Assess the morphology of the red blood cells.
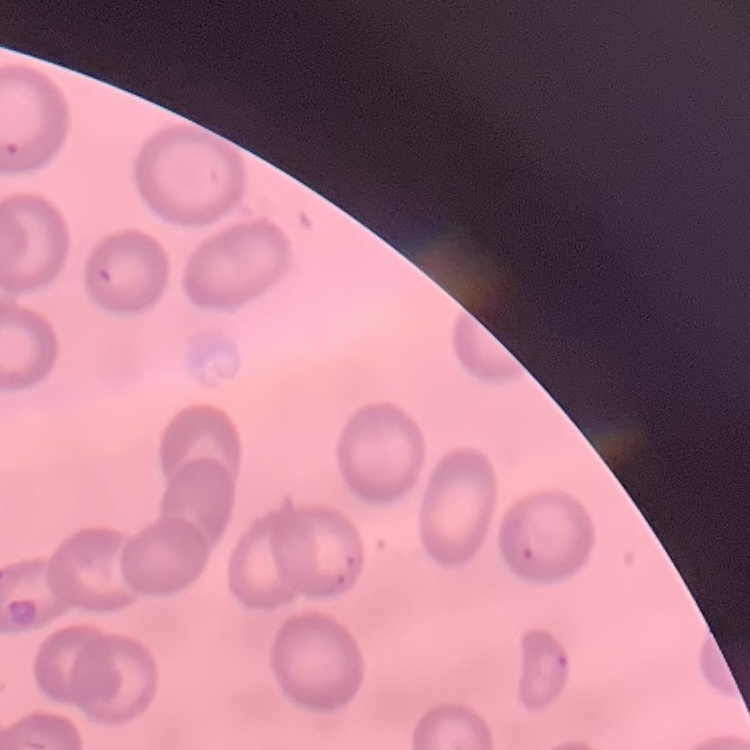
No rouleaux formation.

Square crop of a larger photomicrograph. Thin blood smear. Stained with either Field's or Giemsa.